Draw a bounding box around every parasitised red blood cell.
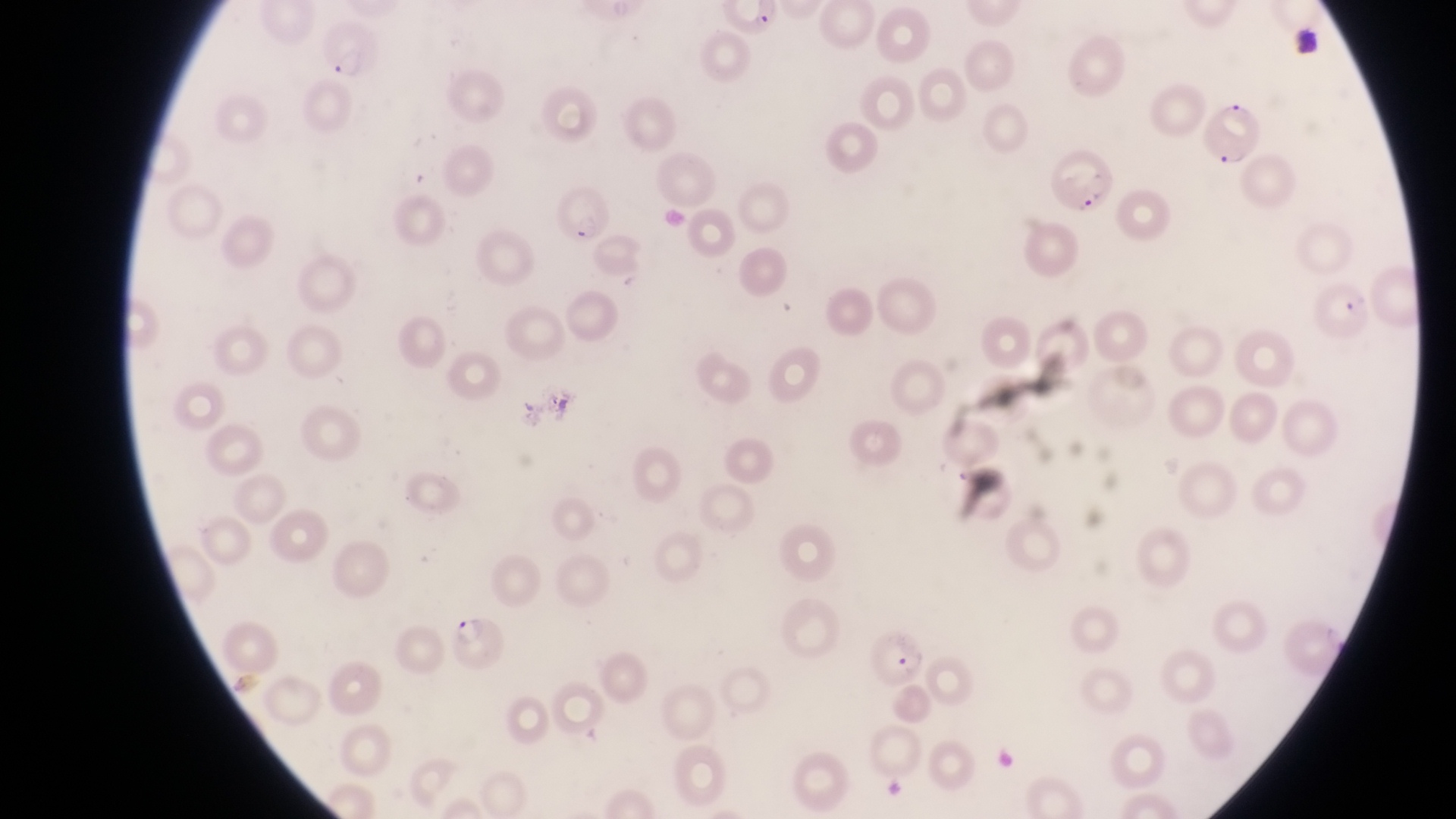

Approximate bounding boxes as left top right bottom in pixels.
Parasitised red blood cells: 320 17 379 84; 1211 95 1264 168; 1050 142 1113 216; 551 187 612 245; 1320 280 1373 336; 447 614 514 675; 862 626 925 687.

One field of view. Image is 1456×819 pixels. Thin blood smear. Collected in Uganda. Captured by a smartphone held over the eyepiece of an Olympus CX-23 microscope. At a magnification of 1000x.